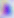
Summary:
  - Identification: Toxoplasma gondii
  - Modality: photomicrograph
  - Magnification: 400x